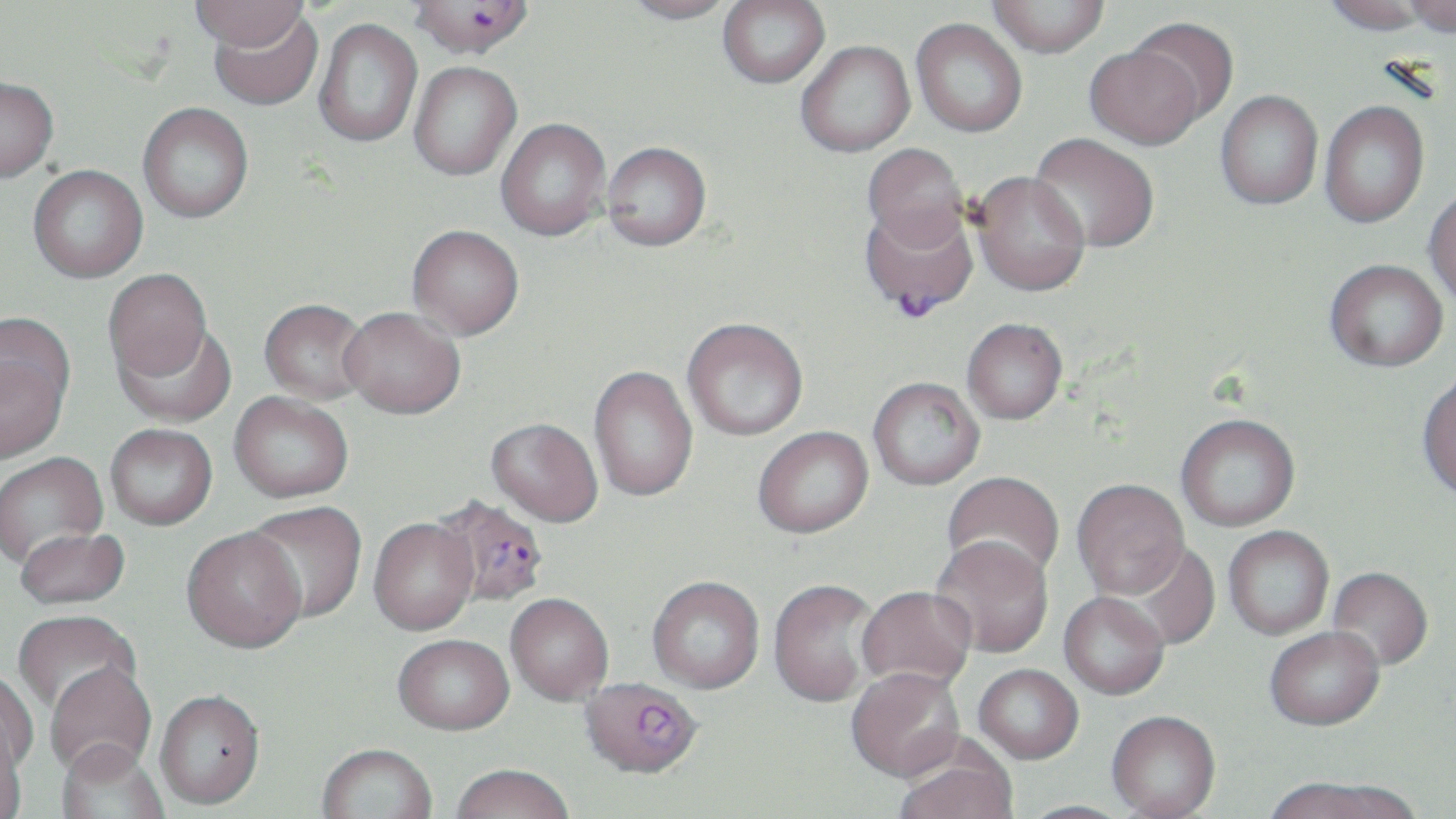
slide-level diagnosis = Plasmodium falciparum
magnification = 1000x
field of view = single
modality = light microscopy
Plasmodium falciparum-infected red blood cell locations = approximate bounding boxes as named x1/y1/x2/y2 corners in pixels: (x1=409, y1=0, x2=534, y2=59), (x1=858, y1=203, x2=979, y2=320), (x1=433, y1=497, x2=549, y2=609), (x1=580, y1=680, x2=703, y2=783)
preparation = thin blood smear
uninfected red blood cell locations = approximate bounding boxes as named x1/y1/x2/y2 corners in pixels: (x1=190, y1=0, x2=308, y2=51), (x1=621, y1=0, x2=737, y2=25), (x1=717, y1=0, x2=830, y2=88), (x1=988, y1=0, x2=1110, y2=58), (x1=1320, y1=0, x2=1432, y2=35), (x1=1402, y1=0, x2=1456, y2=36), (x1=207, y1=7, x2=324, y2=111), (x1=1126, y1=17, x2=1239, y2=126), (x1=911, y1=18, x2=1028, y2=137), (x1=314, y1=19, x2=422, y2=148), (x1=796, y1=40, x2=914, y2=157), (x1=1085, y1=42, x2=1205, y2=149), (x1=409, y1=62, x2=522, y2=181), (x1=0, y1=76, x2=58, y2=182), (x1=1215, y1=90, x2=1323, y2=210), (x1=1320, y1=100, x2=1429, y2=228), (x1=138, y1=102, x2=253, y2=223), (x1=495, y1=118, x2=611, y2=240), (x1=1029, y1=133, x2=1160, y2=254), (x1=601, y1=142, x2=711, y2=251), (x1=863, y1=144, x2=968, y2=253), (x1=28, y1=165, x2=148, y2=282), (x1=972, y1=171, x2=1090, y2=298), (x1=1424, y1=189, x2=1456, y2=308), (x1=407, y1=225, x2=524, y2=340), (x1=1325, y1=259, x2=1449, y2=371), (x1=104, y1=269, x2=212, y2=384), (x1=259, y1=298, x2=371, y2=405), (x1=339, y1=306, x2=466, y2=419), (x1=682, y1=317, x2=808, y2=441), (x1=961, y1=317, x2=1067, y2=424), (x1=114, y1=322, x2=237, y2=428), (x1=0, y1=330, x2=73, y2=463), (x1=589, y1=367, x2=698, y2=504), (x1=1417, y1=371, x2=1456, y2=502), (x1=868, y1=377, x2=984, y2=491), (x1=229, y1=393, x2=354, y2=506), (x1=1175, y1=413, x2=1300, y2=531), (x1=485, y1=420, x2=603, y2=530), (x1=105, y1=425, x2=217, y2=532), (x1=753, y1=428, x2=874, y2=542), (x1=0, y1=453, x2=108, y2=569), (x1=941, y1=472, x2=1064, y2=587), (x1=1072, y1=480, x2=1190, y2=602), (x1=244, y1=501, x2=367, y2=625), (x1=368, y1=520, x2=478, y2=638), (x1=1223, y1=527, x2=1334, y2=641), (x1=15, y1=530, x2=130, y2=614), (x1=181, y1=532, x2=306, y2=658), (x1=930, y1=539, x2=1054, y2=660), (x1=1119, y1=540, x2=1222, y2=650), (x1=1327, y1=568, x2=1433, y2=673), (x1=647, y1=579, x2=764, y2=696), (x1=769, y1=581, x2=880, y2=710), (x1=856, y1=588, x2=976, y2=695), (x1=1058, y1=594, x2=1169, y2=702), (x1=505, y1=596, x2=613, y2=708), (x1=13, y1=611, x2=141, y2=719), (x1=1264, y1=630, x2=1386, y2=735), (x1=392, y1=638, x2=514, y2=739), (x1=45, y1=664, x2=157, y2=784), (x1=973, y1=666, x2=1083, y2=767), (x1=0, y1=670, x2=39, y2=778), (x1=846, y1=670, x2=966, y2=787), (x1=155, y1=693, x2=266, y2=812), (x1=1106, y1=713, x2=1221, y2=819), (x1=1, y1=731, x2=27, y2=819), (x1=893, y1=746, x2=1018, y2=819), (x1=316, y1=747, x2=437, y2=819), (x1=56, y1=749, x2=170, y2=819), (x1=451, y1=768, x2=574, y2=819), (x1=1261, y1=780, x2=1417, y2=819), (x1=1014, y1=801, x2=1140, y2=819)
image size = 1456×819 pixels
stain = May-Grünwald-Giemsa